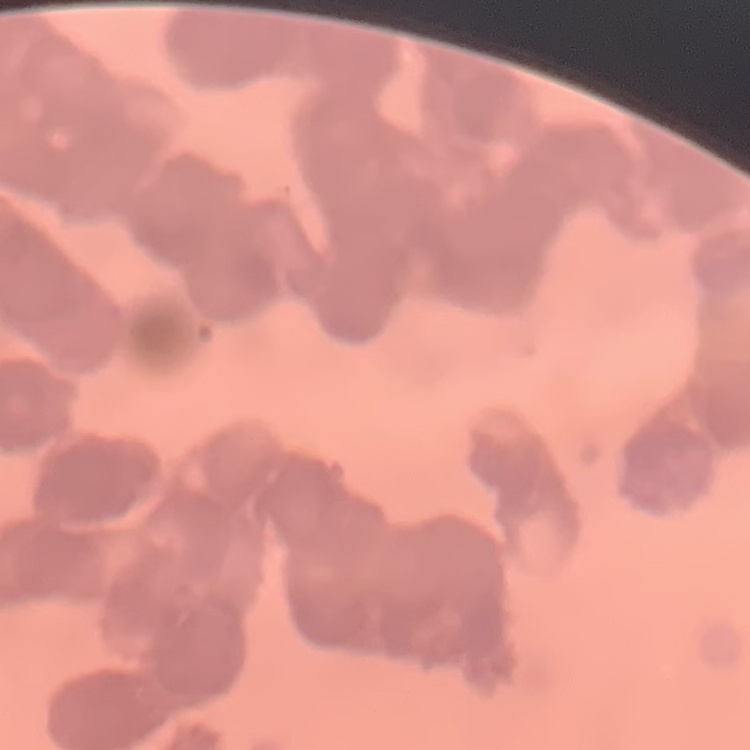

red blood cell morphology = rouleaux formation
stain = Field's or Giemsa
preparation = thin blood film
image type = one tile cut from a larger photomicrograph